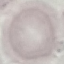

malaria status = uninfected
preparation = thin blood smear
stain = Giemsa
capture = smartphone through the microscope eyepiece
image type = automatically extracted cell patch, resized to 64 × 64 pixels